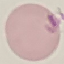
Summary:
  - Result: no malaria parasites seen
  - Stain: Giemsa
  - Capture: smartphone through the microscope eyepiece
  - Image type: cell patch, automatically extracted from a larger field of view and resized to 64 × 64 pixels
  - Preparation: thin blood film